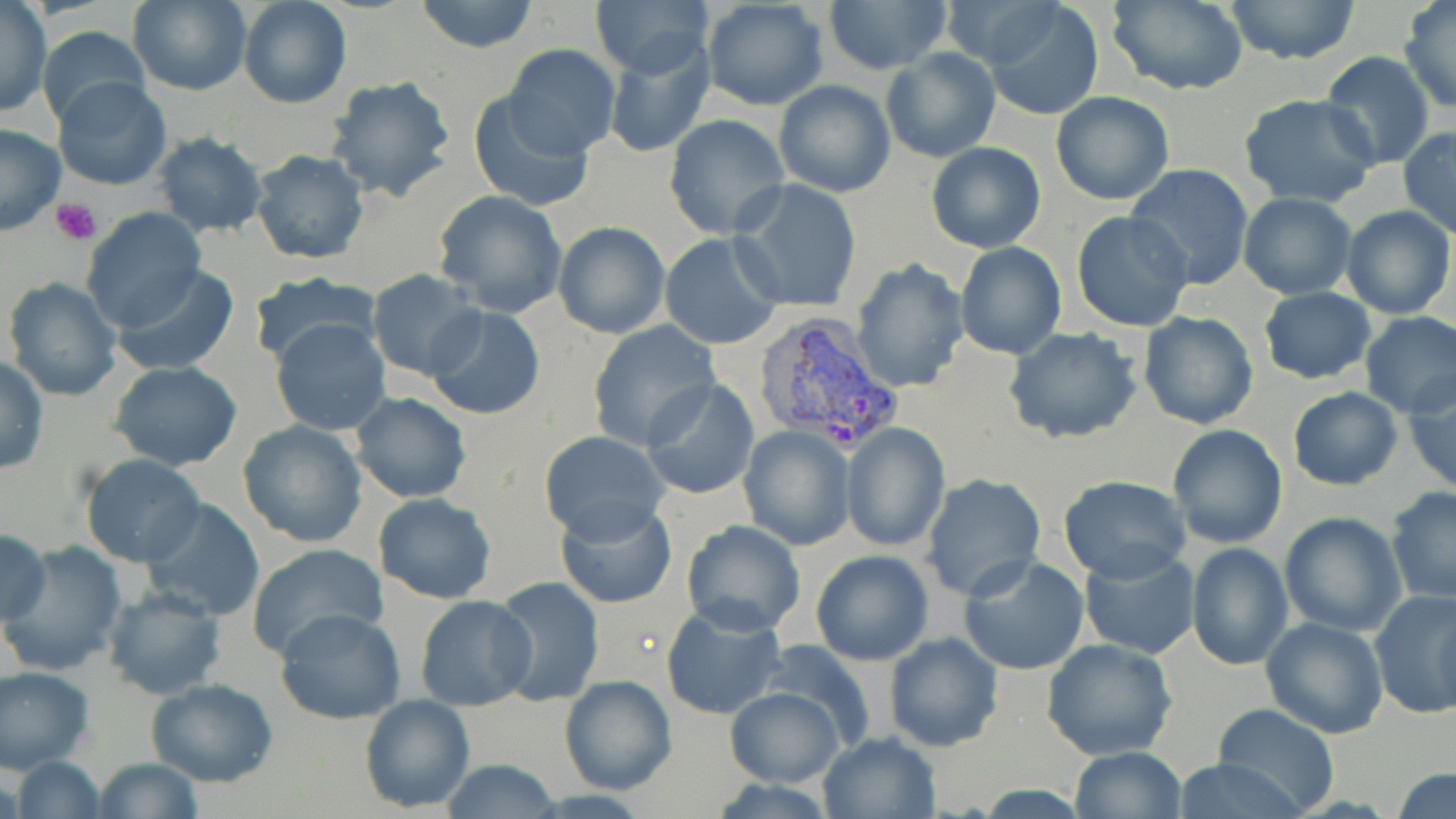
Summary:
  - Coordinate format: approximate bounding boxes as (x1, y1, x2, y2) in pixels
  - Uninfected red blood cell locations: (129, 0, 252, 96), (238, 0, 351, 110), (414, 0, 540, 53), (589, 0, 715, 78), (824, 0, 951, 73), (938, 0, 1064, 67), (1220, 0, 1365, 67), (701, 1, 829, 111), (1106, 1, 1249, 94), (980, 2, 1104, 119), (1400, 2, 1456, 113), (0, 4, 49, 117), (39, 26, 150, 129), (601, 38, 715, 159), (505, 44, 621, 157), (880, 48, 1001, 163), (1320, 51, 1435, 169), (54, 77, 172, 191), (325, 77, 458, 203), (773, 80, 895, 198), (467, 92, 596, 213), (1051, 92, 1177, 205), (1237, 93, 1382, 207), (663, 113, 792, 240), (0, 124, 66, 235), (1399, 126, 1456, 237), (152, 132, 265, 238), (925, 142, 1048, 254), (250, 148, 370, 266), (1125, 163, 1255, 289), (730, 179, 863, 315), (432, 190, 567, 317), (1238, 193, 1356, 300), (1341, 205, 1454, 320), (81, 208, 206, 332), (1071, 211, 1195, 332), (553, 220, 670, 338), (659, 232, 784, 350), (955, 241, 1068, 361), (851, 258, 969, 395), (113, 265, 238, 377), (368, 269, 483, 381), (249, 271, 379, 367), (4, 277, 123, 401), (1257, 287, 1378, 384), (424, 306, 546, 420), (1136, 310, 1260, 429), (1358, 310, 1456, 419), (270, 319, 392, 437), (587, 321, 721, 449), (1005, 327, 1144, 445), (0, 358, 49, 473), (108, 361, 243, 471), (1404, 369, 1455, 494), (640, 379, 759, 500), (1286, 387, 1404, 492), (351, 392, 472, 505), (237, 420, 368, 547), (840, 422, 951, 551), (1167, 423, 1289, 549), (737, 426, 854, 551), (537, 429, 668, 540), (79, 454, 206, 569), (919, 473, 1047, 601), (1058, 475, 1193, 584), (1385, 486, 1456, 603), (373, 493, 497, 605), (139, 499, 266, 622), (554, 499, 675, 609), (1280, 511, 1406, 635), (681, 521, 805, 636), (0, 528, 51, 627), (1, 542, 127, 674), (1185, 542, 1294, 670), (247, 544, 387, 659), (1078, 546, 1200, 660), (810, 549, 934, 666), (957, 556, 1091, 676), (489, 576, 605, 707), (102, 586, 227, 700), (1370, 588, 1456, 719), (415, 595, 537, 712), (659, 601, 787, 720), (275, 609, 406, 725), (1261, 617, 1388, 738), (883, 632, 1003, 752), (1041, 637, 1177, 760), (756, 640, 877, 751), (0, 665, 94, 774), (558, 673, 677, 796), (144, 678, 278, 786), (723, 687, 845, 786), (359, 693, 476, 814), (1211, 703, 1342, 815), (818, 730, 943, 819), (1067, 747, 1187, 819), (11, 757, 105, 818), (92, 757, 205, 819), (1172, 757, 1314, 819), (436, 760, 566, 817), (1391, 768, 1456, 819)
  - Platelet locations: (50, 197, 102, 246)
  - Plasmodium vivax-infected red blood cell locations: (750, 314, 902, 454)
  - Slide-level diagnosis: Plasmodium vivax
  - Preparation: thin blood film
  - Stain: May-Grünwald-Giemsa
  - Modality: light microscopy
  - Magnification: 1000x
  - Field of view: one of a larger specimen
  - Image size: 1456×819 pixels